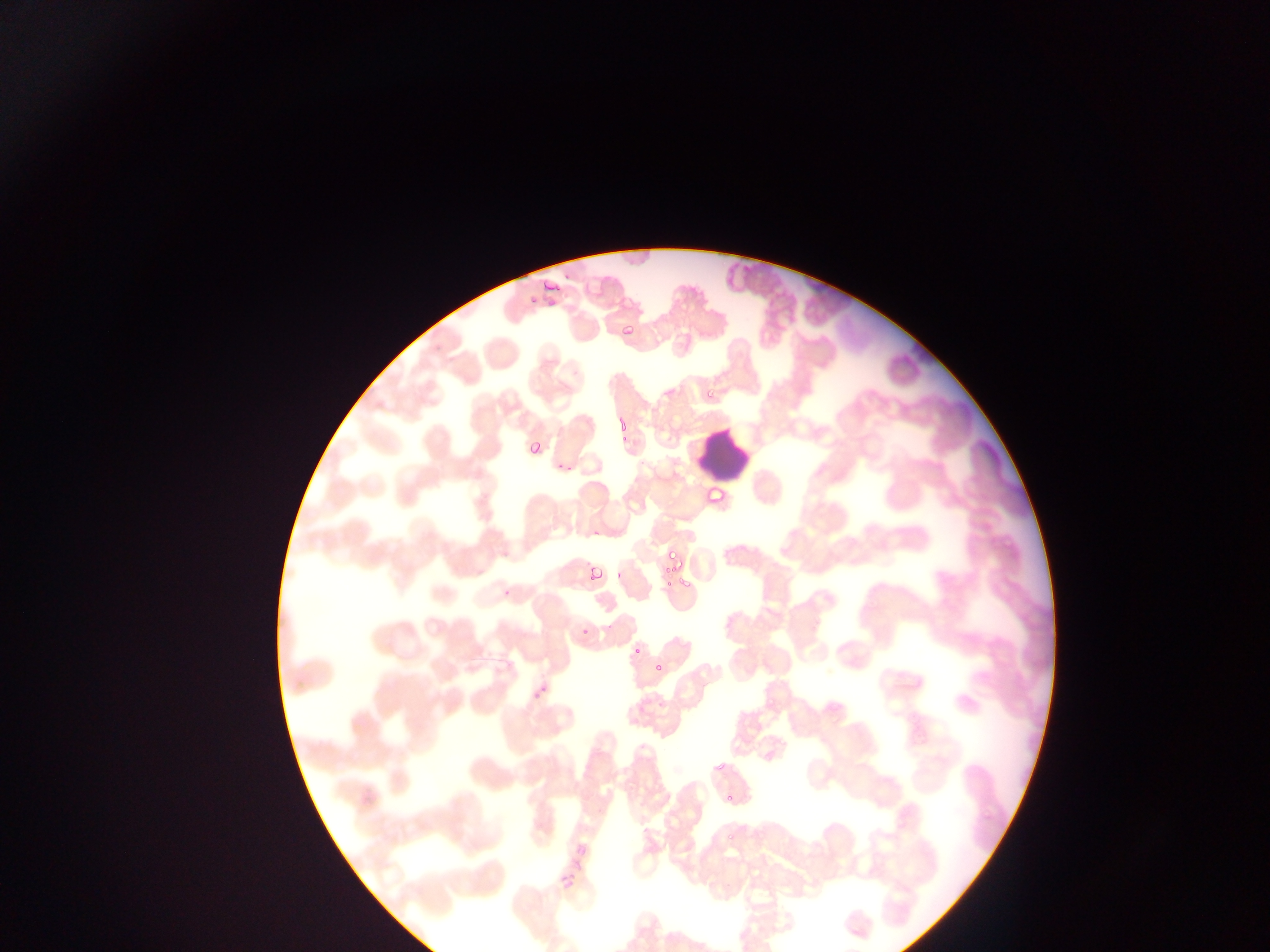

Approximate bounding boxes as {left, top, right, bottom} in pixels. Leukocyte locations: {697, 427, 753, 483}, {834, 906, 881, 947}. Plasmodium parasite locations: {537, 273, 569, 292}, {619, 306, 637, 350}, {701, 384, 721, 395}, {616, 415, 630, 433}, {526, 429, 555, 455}, {703, 482, 728, 505}, {586, 541, 612, 584}, {663, 542, 685, 561}, {660, 557, 692, 591}, {620, 636, 636, 654}, {651, 661, 666, 676}, {531, 665, 568, 698}, {723, 790, 738, 807}, {555, 817, 628, 894}. Collected in Ghana. Image is 1270×952 pixels. One field of view. Thin blood film. Photographed through a microscope with a mobile-phone camera.